Report the malaria status of this cell.
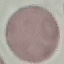

Uninfected.

Summary:
  - Preparation: thin smear
  - Capture: smartphone camera at the microscope eyepiece
  - Image type: automatically extracted cell patch, resized to 64 × 64 pixels
  - Stain: Giemsa